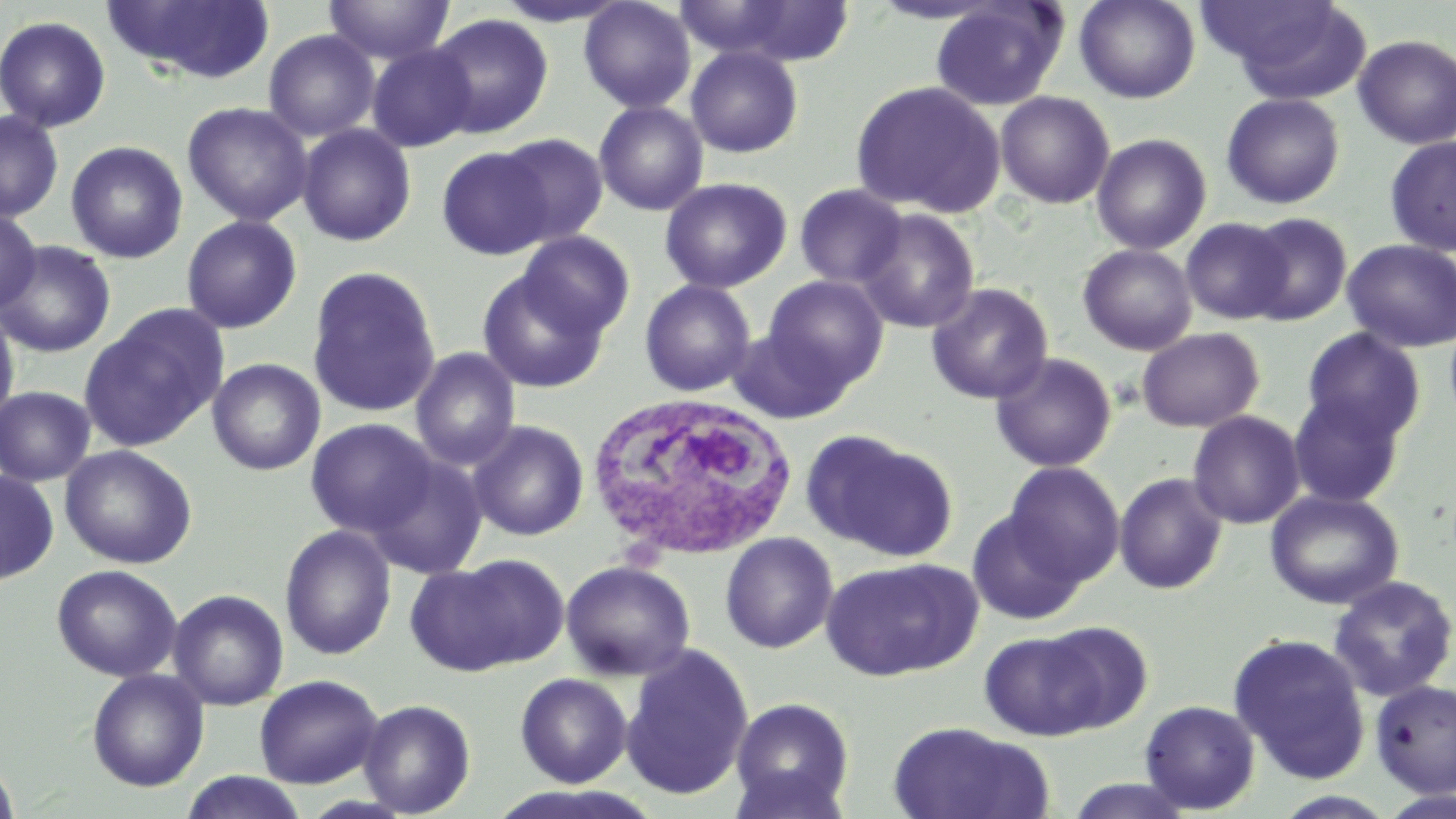

Approximate bounding boxes as named x1/y1/x2/y2 corners in pixels. White blood cell locations: (x1=584, y1=391, x2=802, y2=561). Uninfected red blood cell locations: (x1=104, y1=0, x2=276, y2=84), (x1=323, y1=0, x2=455, y2=65), (x1=492, y1=0, x2=632, y2=27), (x1=578, y1=0, x2=696, y2=113), (x1=677, y1=0, x2=857, y2=66), (x1=1074, y1=0, x2=1200, y2=104), (x1=1200, y1=0, x2=1370, y2=99), (x1=930, y1=1, x2=1068, y2=111), (x1=426, y1=13, x2=554, y2=139), (x1=0, y1=15, x2=112, y2=133), (x1=263, y1=30, x2=380, y2=141), (x1=1353, y1=34, x2=1456, y2=150), (x1=366, y1=43, x2=478, y2=152), (x1=685, y1=46, x2=804, y2=158), (x1=850, y1=80, x2=1005, y2=217), (x1=995, y1=91, x2=1114, y2=209), (x1=1221, y1=93, x2=1345, y2=209), (x1=182, y1=101, x2=313, y2=226), (x1=593, y1=101, x2=709, y2=216), (x1=0, y1=110, x2=63, y2=222), (x1=297, y1=123, x2=417, y2=247), (x1=495, y1=133, x2=608, y2=246), (x1=1092, y1=134, x2=1211, y2=254), (x1=1384, y1=137, x2=1456, y2=256), (x1=65, y1=140, x2=188, y2=263), (x1=436, y1=146, x2=553, y2=259), (x1=659, y1=177, x2=792, y2=293), (x1=794, y1=184, x2=908, y2=289), (x1=0, y1=208, x2=41, y2=313), (x1=855, y1=209, x2=980, y2=333), (x1=1243, y1=212, x2=1352, y2=325), (x1=181, y1=215, x2=302, y2=334), (x1=1180, y1=218, x2=1293, y2=325), (x1=517, y1=230, x2=634, y2=339), (x1=1342, y1=239, x2=1456, y2=353), (x1=0, y1=240, x2=116, y2=358), (x1=1078, y1=243, x2=1197, y2=356), (x1=306, y1=265, x2=442, y2=418), (x1=477, y1=269, x2=609, y2=394), (x1=762, y1=275, x2=888, y2=389), (x1=639, y1=279, x2=757, y2=397), (x1=925, y1=283, x2=1054, y2=404), (x1=79, y1=304, x2=227, y2=450), (x1=0, y1=305, x2=20, y2=429), (x1=1444, y1=314, x2=1456, y2=427), (x1=727, y1=325, x2=853, y2=424), (x1=1137, y1=327, x2=1264, y2=432), (x1=1302, y1=328, x2=1426, y2=444), (x1=410, y1=348, x2=521, y2=471), (x1=990, y1=352, x2=1117, y2=472), (x1=208, y1=358, x2=325, y2=476), (x1=0, y1=386, x2=96, y2=486), (x1=1288, y1=391, x2=1406, y2=508), (x1=1187, y1=411, x2=1305, y2=529), (x1=306, y1=418, x2=437, y2=538), (x1=467, y1=420, x2=589, y2=541), (x1=804, y1=430, x2=955, y2=560), (x1=59, y1=445, x2=197, y2=569), (x1=365, y1=453, x2=488, y2=580), (x1=1004, y1=462, x2=1125, y2=586), (x1=0, y1=469, x2=59, y2=586), (x1=1114, y1=472, x2=1228, y2=595), (x1=1264, y1=490, x2=1404, y2=609), (x1=967, y1=509, x2=1086, y2=625), (x1=279, y1=525, x2=397, y2=660), (x1=720, y1=532, x2=838, y2=654), (x1=409, y1=554, x2=565, y2=675), (x1=820, y1=557, x2=981, y2=682), (x1=561, y1=560, x2=696, y2=681), (x1=52, y1=564, x2=182, y2=682), (x1=1327, y1=576, x2=1455, y2=702), (x1=168, y1=589, x2=289, y2=711), (x1=1038, y1=621, x2=1153, y2=731), (x1=979, y1=631, x2=1108, y2=740), (x1=1228, y1=634, x2=1370, y2=784), (x1=619, y1=644, x2=755, y2=801), (x1=86, y1=668, x2=209, y2=792), (x1=515, y1=673, x2=632, y2=787), (x1=254, y1=674, x2=383, y2=788), (x1=1370, y1=679, x2=1456, y2=798), (x1=730, y1=697, x2=855, y2=817), (x1=357, y1=698, x2=476, y2=817), (x1=1139, y1=700, x2=1260, y2=814), (x1=886, y1=721, x2=1051, y2=819), (x1=0, y1=759, x2=19, y2=819), (x1=726, y1=764, x2=853, y2=819), (x1=178, y1=771, x2=310, y2=819), (x1=1063, y1=777, x2=1198, y2=818), (x1=1378, y1=789, x2=1456, y2=817), (x1=1271, y1=791, x2=1400, y2=818). Slide-level diagnosis: negative for blood parasites. Thin blood smear. One field of a larger specimen. Optical microscopy. Image is 1456×819 pixels. May-Grünwald-Giemsa stain. Captured at 1000x magnification.